Report the malaria status of this cell.
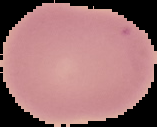

Uninfected.

Cell region segmented out of the field of view; the surrounding area is masked to black. Image is 157×127 pixels. From a thin blood smear.